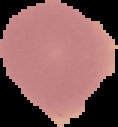
image size = 118×127 pixels
result = no Plasmodium parasites seen
image type = segmented cell region with the area outside set to black
preparation = thin blood film